Report the malaria status of this cell.
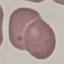

It is uninfected.

image type = automatically extracted cell patch, resized to 64 × 64 pixels
stain = Giemsa
capture = smartphone camera at the microscope eyepiece
preparation = thin blood film